Assess this cell for malaria.
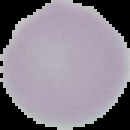
It is uninfected.

{
  "image_size": "130×130 pixels",
  "preparation": "thin blood smear",
  "image_type": "segmented cell region with the area outside set to black"
}